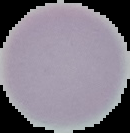

Summary:
  - Image type: segmented cell region on a black background
  - Malaria status: uninfected
  - Image size: 130×133 pixels
  - Preparation: thin blood smear